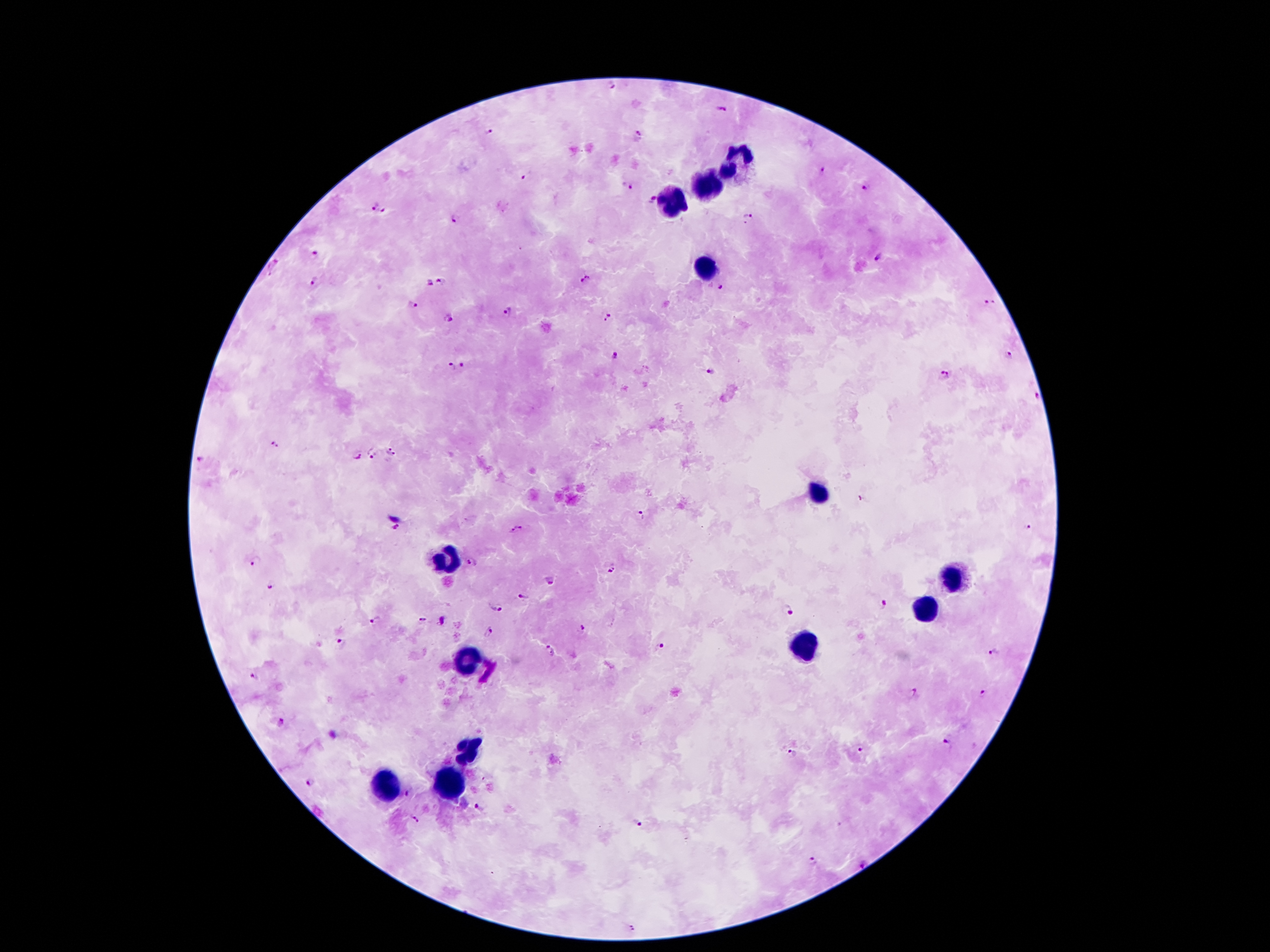
Approximate centers as [x, y] in pixels. Leukocyte locations: [738, 162], [710, 184], [672, 202], [705, 265], [818, 493], [447, 562], [955, 577], [924, 610], [807, 644], [466, 657], [464, 752], [382, 785], [447, 787]. Malaria parasite locations: [613, 86], [720, 109], [489, 132], [638, 135], [822, 170], [526, 177], [627, 186], [864, 187], [652, 200], [373, 206], [385, 210], [749, 215], [455, 217], [315, 254], [879, 258], [274, 265], [585, 279], [313, 280], [442, 282], [429, 283], [716, 287], [990, 303], [414, 304], [507, 311], [610, 316], [448, 318], [614, 356], [1010, 356], [450, 366], [465, 366], [709, 373], [946, 375], [1036, 394], [275, 446], [390, 450], [371, 454], [358, 456], [201, 460], [862, 498], [642, 515], [521, 526], [395, 527], [1028, 528], [511, 533], [256, 562], [473, 562], [610, 567], [550, 580], [269, 586], [523, 597], [883, 603], [497, 607], [789, 609], [374, 620], [423, 620], [582, 629], [488, 632], [342, 643], [660, 645], [549, 652], [994, 654], [256, 676], [913, 693], [982, 693], [282, 721], [947, 744], [862, 751], [792, 753], [311, 782], [410, 793], [479, 809], [415, 818], [636, 824], [814, 861], [862, 862], [634, 929]. 100x magnification. Single field of view. Smartphone photograph taken through the microscope eyepiece. Giemsa stain. Image is 1270×952 pixels. Thick peripheral-blood smear. Patient malaria status: infected with Plasmodium falciparum.